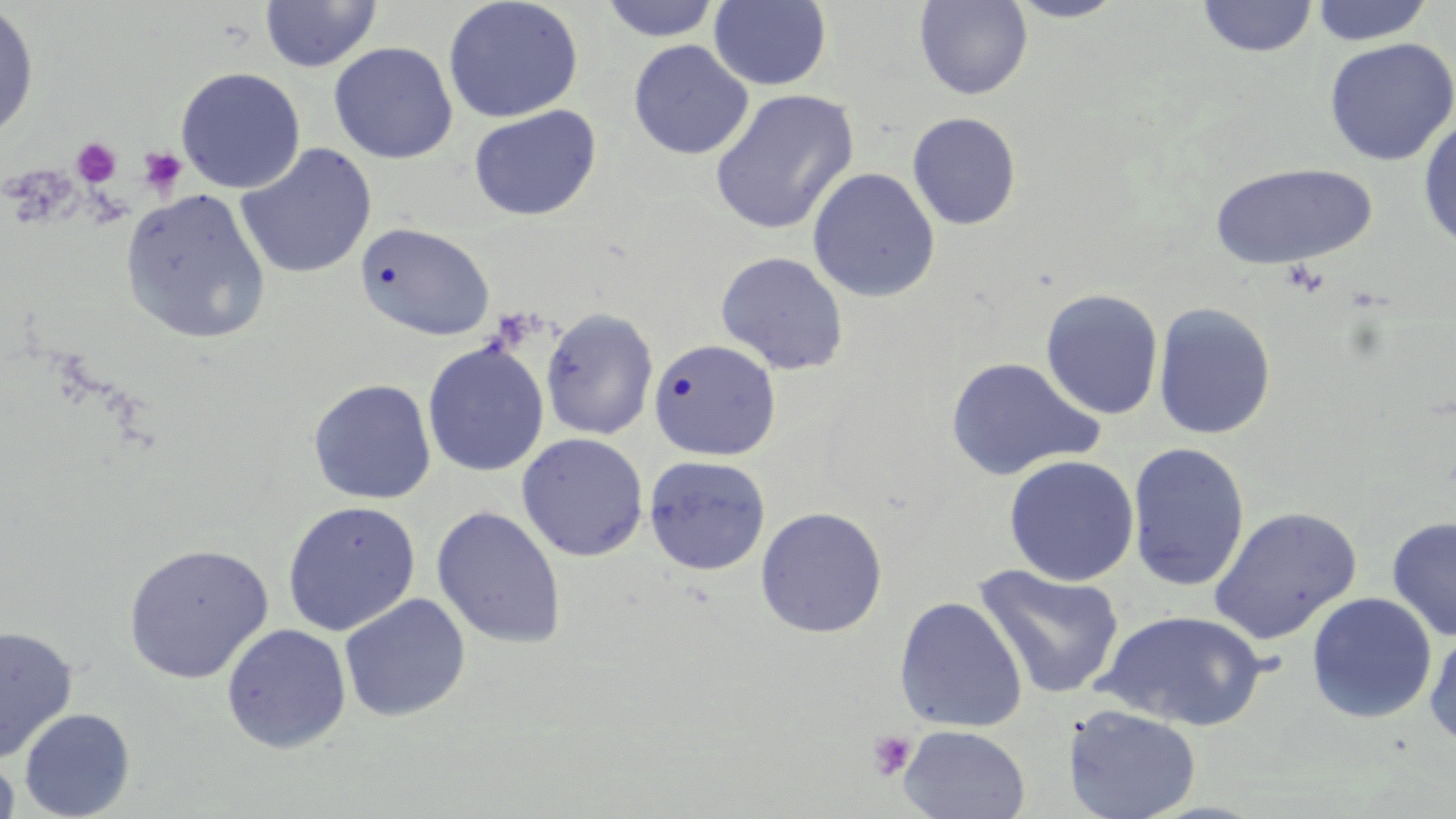
slide-level diagnosis = no evidence of blood parasites
field of view = one of a larger specimen
modality = optical microscopy
uninfected red blood cell locations = approximate bounding boxes as named x1/y1/x2/y2 corners in pixels: (x1=258, y1=0, x2=382, y2=73), (x1=442, y1=0, x2=584, y2=123), (x1=708, y1=0, x2=832, y2=90), (x1=913, y1=0, x2=1033, y2=100), (x1=1005, y1=0, x2=1128, y2=23), (x1=1195, y1=0, x2=1318, y2=59), (x1=1308, y1=0, x2=1436, y2=46), (x1=599, y1=1, x2=722, y2=42), (x1=0, y1=3, x2=39, y2=142), (x1=1324, y1=37, x2=1456, y2=167), (x1=628, y1=39, x2=754, y2=159), (x1=329, y1=41, x2=458, y2=164), (x1=175, y1=67, x2=305, y2=194), (x1=709, y1=88, x2=859, y2=236), (x1=468, y1=105, x2=601, y2=221), (x1=907, y1=112, x2=1022, y2=230), (x1=1417, y1=116, x2=1456, y2=250), (x1=235, y1=143, x2=376, y2=280), (x1=1208, y1=162, x2=1377, y2=270), (x1=806, y1=167, x2=941, y2=302), (x1=119, y1=188, x2=271, y2=344), (x1=354, y1=222, x2=496, y2=341), (x1=715, y1=251, x2=849, y2=375), (x1=1041, y1=288, x2=1164, y2=420), (x1=1153, y1=302, x2=1276, y2=440), (x1=540, y1=307, x2=658, y2=440), (x1=648, y1=338, x2=781, y2=460), (x1=422, y1=341, x2=548, y2=477), (x1=945, y1=356, x2=1105, y2=482), (x1=308, y1=378, x2=436, y2=504), (x1=516, y1=432, x2=649, y2=562), (x1=1126, y1=442, x2=1250, y2=593), (x1=1003, y1=454, x2=1140, y2=586), (x1=643, y1=455, x2=771, y2=575), (x1=282, y1=500, x2=421, y2=636), (x1=431, y1=504, x2=567, y2=650), (x1=755, y1=506, x2=888, y2=638), (x1=1208, y1=507, x2=1362, y2=646), (x1=1386, y1=516, x2=1456, y2=642), (x1=122, y1=542, x2=273, y2=683), (x1=973, y1=563, x2=1125, y2=701), (x1=1306, y1=592, x2=1437, y2=724), (x1=339, y1=593, x2=471, y2=722), (x1=893, y1=596, x2=1028, y2=733), (x1=1096, y1=610, x2=1267, y2=731), (x1=222, y1=623, x2=351, y2=753), (x1=0, y1=625, x2=78, y2=765), (x1=1424, y1=625, x2=1456, y2=750), (x1=1062, y1=704, x2=1201, y2=819), (x1=18, y1=708, x2=136, y2=819), (x1=898, y1=724, x2=1030, y2=819), (x1=0, y1=753, x2=20, y2=818)
magnification = 1000x
platelet locations = approximate bounding boxes as named x1/y1/x2/y2 corners in pixels: (x1=70, y1=136, x2=122, y2=188), (x1=138, y1=147, x2=188, y2=197), (x1=867, y1=729, x2=917, y2=781)
stain = May-Grünwald-Giemsa
preparation = thin blood film
image size = 1456×819 pixels